Locate every Plasmodium parasite.
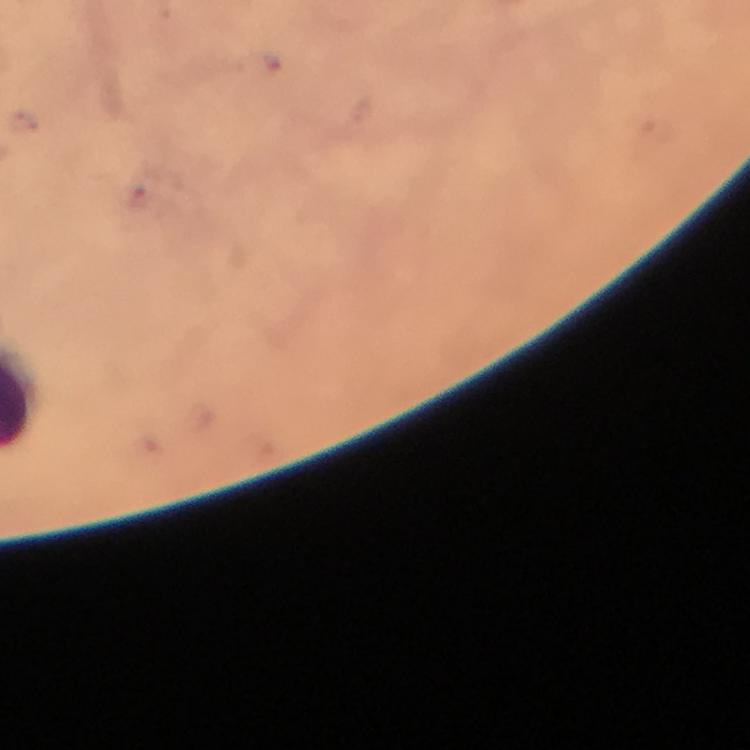

Approximate centers as {x, y} in pixels.
Plasmodium parasites: {140, 200}.

preparation = thick smear
cropped from = a single field of view
stain = Giemsa
capture = smartphone camera through the microscope
immersion oil = applied
magnification = 100x
context = from a malaria diagnostic workup
image size = 750×750 pixels